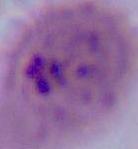

Summary:
  - Modality: micrograph
  - Identification: Plasmodium
  - Magnification: 400x or 1000x